Identify the parasite.
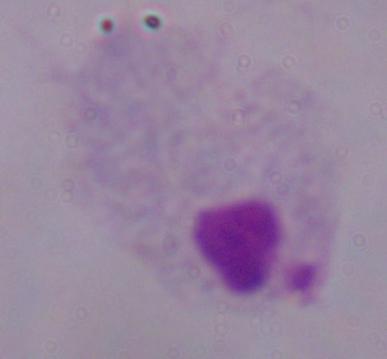
A trichomonad.

1000x magnification. Micrograph.